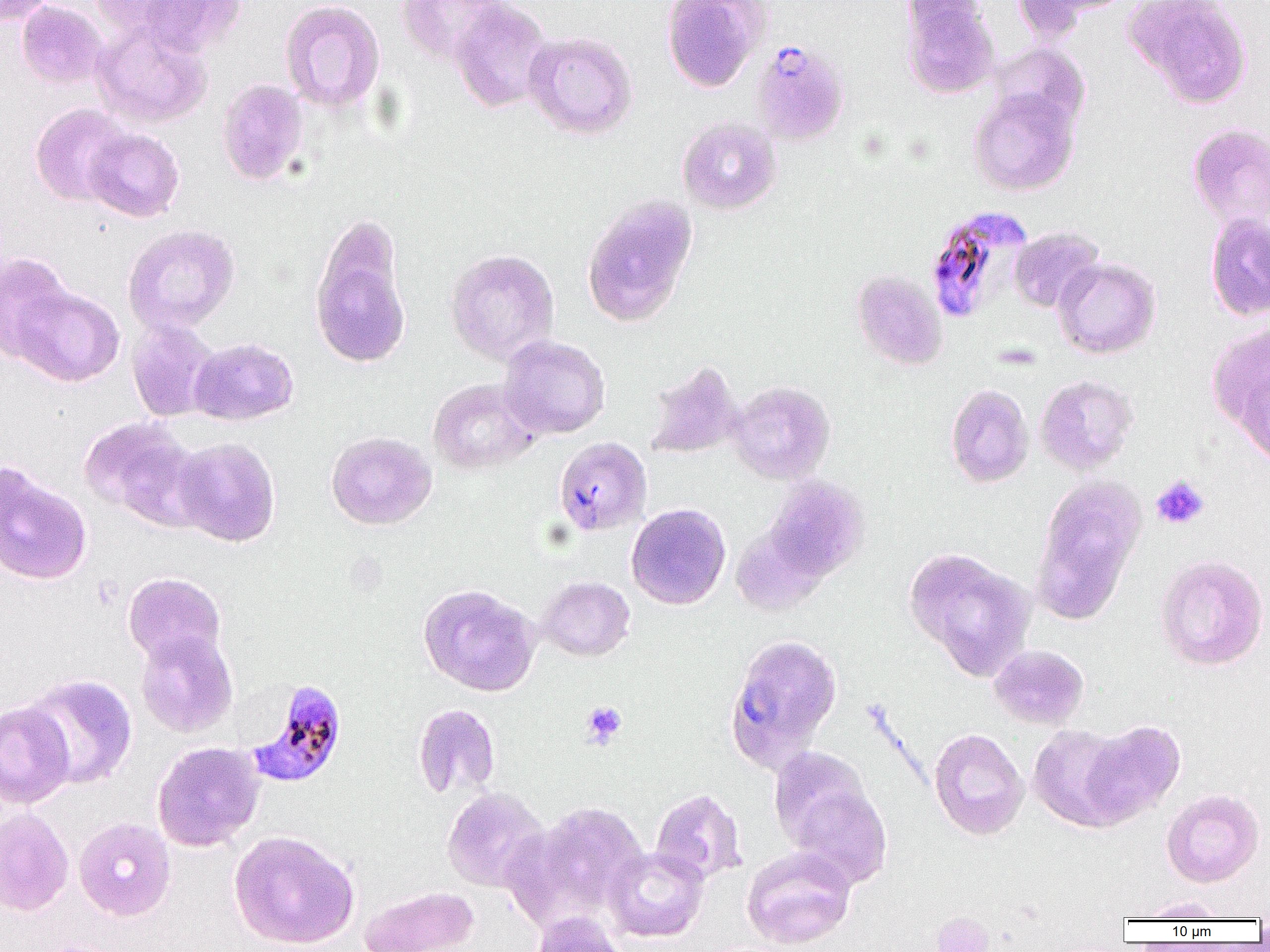

slide_level_diagnosis: Plasmodium falciparum
field_of_view: one of a larger specimen
modality: light microscopy
magnification: 1000x
preparation: thin blood smear
platelet_locations_subset: 'approximate bounding boxes as (x1, y1, x2, y2) in pixels: (1151, 476, 1209, 529), (581, 701, 627, 748)'
image_size: 1270×952 pixels
plasmodium_falciparum_infected_red_blood_cell_locations: 'approximate bounding boxes as (x1, y1, x2, y2) in pixels: (752, 35, 851, 141), (924, 205, 1032, 323), (247, 679, 347, 787)'
uninfected_red_blood_cell_locations_subset: 'approximate bounding boxes as (x1, y1, x2, y2) in pixels: (1, 0, 56, 24), (87, 0, 212, 43), (397, 0, 509, 65), (661, 0, 769, 93), (1011, 0, 1101, 43), (1123, 0, 1253, 107), (16, 1, 107, 88), (133, 1, 247, 56), (280, 1, 385, 113), (449, 1, 553, 113), (901, 1, 1000, 99), (91, 18, 213, 128), (524, 31, 638, 140), (989, 43, 1091, 131), (217, 78, 310, 186), (968, 88, 1079, 196), (30, 103, 133, 207), (677, 116, 782, 214), (1187, 123, 1270, 231), (84, 127, 184, 222), (581, 195, 699, 328), (1205, 211, 1270, 321), (123, 224, 240, 334), (1009, 226, 1105, 313), (310, 233, 412, 370), (445, 249, 560, 365), (0, 251, 75, 363), (1053, 257, 1161, 359), (851, 269, 949, 371), (11, 284, 124, 388), (127, 317, 220, 422), (1206, 324, 1270, 438), (498, 335, 611, 439), (190, 337, 298, 425), (644, 360, 744, 459), (1233, 361, 1270, 470), (1035, 375, 1139, 475), (428, 378, 540, 474), (728, 380, 835, 484), (946, 383, 1034, 487), (79, 417, 203, 526), (325, 431, 436, 530), (172, 437, 281, 547), (554, 437, 652, 535), (0, 462, 93, 586), (766, 476, 869, 579), (1034, 479, 1145, 617), (626, 503, 731, 610), (904, 546, 1036, 679), (1154, 553, 1269, 671), (122, 572, 226, 666), (537, 576, 636, 661), (418, 583, 541, 696), (135, 630, 238, 738), (723, 633, 842, 773), (989, 644, 1089, 730), (22, 674, 138, 789), (0, 701, 75, 809), (413, 703, 500, 799), (1078, 719, 1185, 826), (1027, 725, 1131, 831), (928, 728, 1029, 840), (151, 741, 265, 852), (768, 746, 872, 850), (789, 785, 892, 888), (441, 787, 550, 893), (650, 788, 747, 885), (1162, 788, 1264, 887), (527, 802, 648, 918), (0, 808, 73, 916), (74, 818, 175, 920), (229, 830, 360, 949), (741, 846, 856, 949), (604, 847, 709, 942), (361, 886, 479, 952), (1132, 896, 1231, 921), (529, 912, 628, 952), (29, 938, 127, 952)'